State which cell type is depicted.
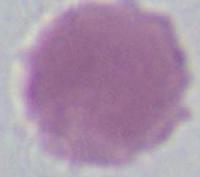
This is an erythrocyte.

Photomicrograph. Captured at 1000x magnification.